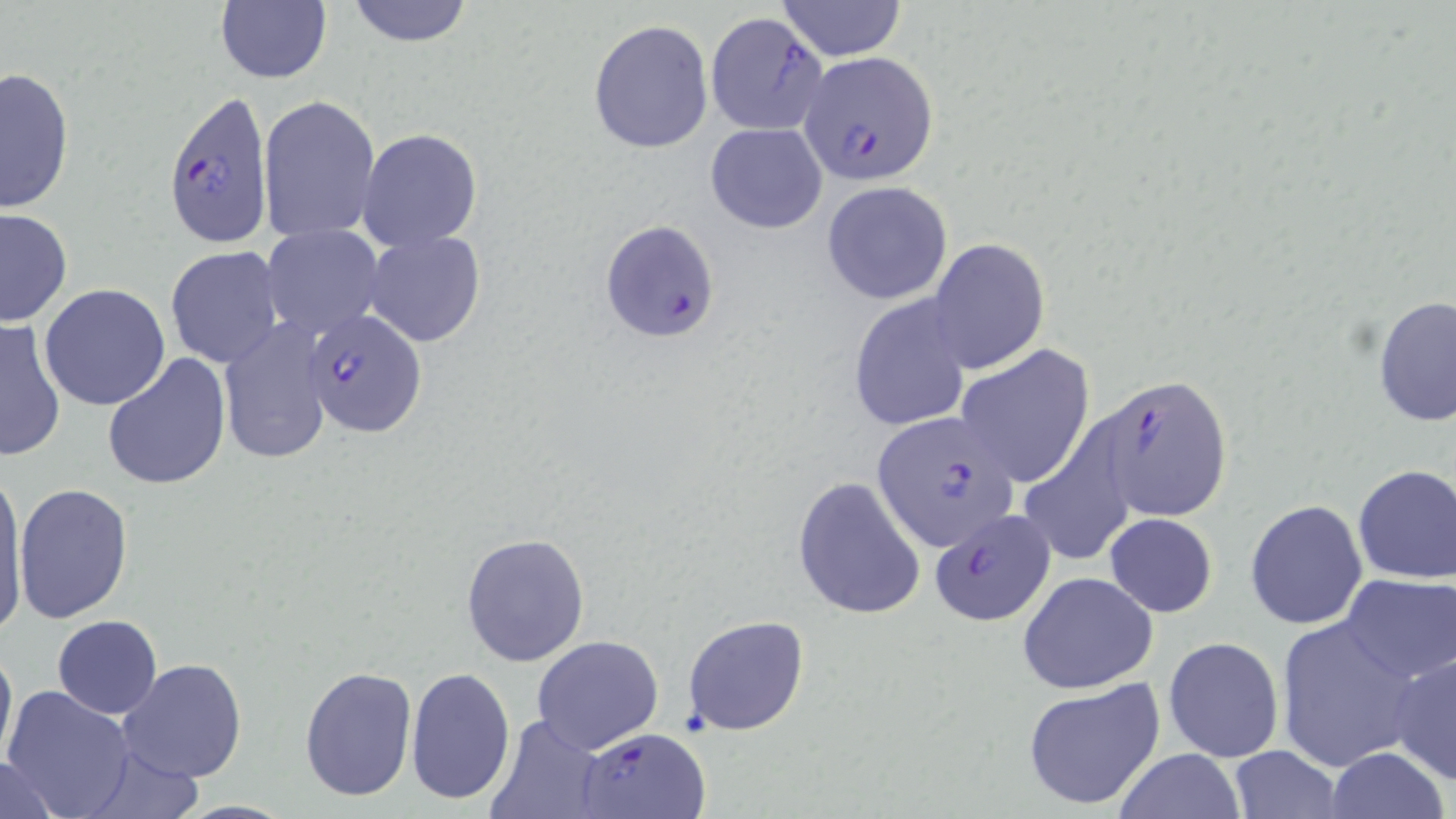

Approximate bounding boxes as (x1,y1)-(x2,y2) corner pairs in pixels. Uninfected red blood cell locations: (343,0)-(477,47), (777,1)-(908,60), (214,2)-(332,85), (588,19)-(713,155), (1,66)-(74,213), (257,95)-(380,242), (706,122)-(827,233), (358,129)-(482,251), (821,181)-(953,305), (0,207)-(72,326), (261,226)-(384,340), (363,231)-(486,347), (926,237)-(1050,375), (164,245)-(285,369), (39,284)-(171,411), (848,293)-(975,434), (1373,296)-(1456,427), (0,318)-(67,462), (214,319)-(334,464), (955,344)-(1096,488), (102,352)-(231,491), (1019,406)-(1136,564), (1353,464)-(1456,585), (0,468)-(31,634), (792,474)-(928,621), (12,483)-(133,623), (1244,499)-(1368,631), (1105,514)-(1218,618), (460,532)-(590,668), (1018,571)-(1159,695), (1340,574)-(1456,683), (683,614)-(811,737), (52,615)-(162,719), (1275,615)-(1425,770), (532,636)-(663,754), (1163,636)-(1284,762), (0,638)-(16,772), (1388,649)-(1455,784), (116,658)-(248,783), (299,664)-(417,799), (406,666)-(515,806), (1021,678)-(1169,813), (3,685)-(137,818), (485,714)-(611,819), (1229,744)-(1342,818), (1324,747)-(1450,818), (1116,749)-(1244,819), (0,754)-(65,819), (167,799)-(298,817). Plasmodium falciparum-infected red blood cell locations: (704,12)-(829,135), (799,52)-(938,186), (162,88)-(272,249), (601,218)-(720,342), (305,307)-(428,437), (1096,376)-(1232,523), (873,415)-(1018,548), (927,508)-(1056,627), (580,727)-(708,819). Slide-level diagnosis: Plasmodium falciparum. Optical microscopy. Thin blood film. Single field of view. Captured at 1000x magnification. Image is 1456×819 pixels. May-Grünwald-Giemsa stain.